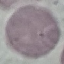
malaria status = uninfected
preparation = thin smear
stain = Giemsa
image type = automatically extracted cell patch, resized to 64 × 64 pixels
capture = smartphone camera at the microscope eyepiece